Assess this cell for malaria.
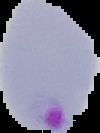
Parasitized.

Summary:
  - Preparation: thin blood smear
  - Image size: 100×133 pixels
  - Image type: segmented cell region on a black background